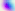
Micrograph. Captured at 400x magnification. Toxoplasma gondii is shown.